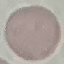 Malaria status: uninfected. Automatically extracted cell patch, resized to 64 × 64 pixels. Photographed with a smartphone camera at the microscope eyepiece. Thin blood smear. Giemsa-stained preparation.